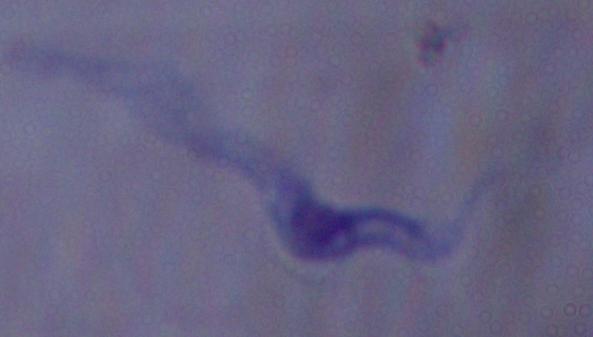

modality = micrograph
identification = trypanosome
magnification = 1000x